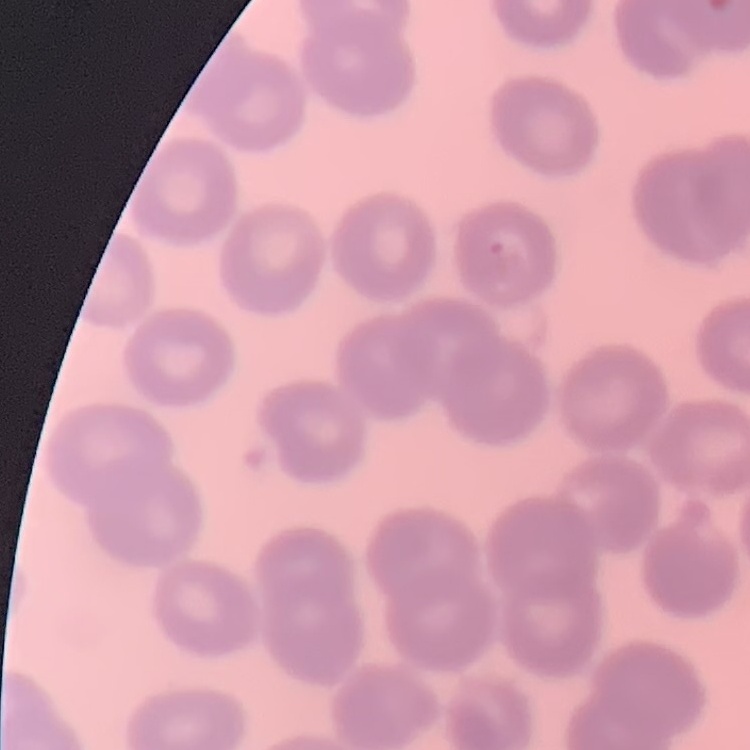

erythrocyte morphology = no rouleaux formation
preparation = thin blood film
stain = Field's or Giemsa
image type = square crop of a larger photomicrograph